Identify the cell.
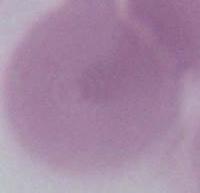

This is an erythrocyte.

Summary:
  - Magnification: 1000x
  - Modality: micrograph